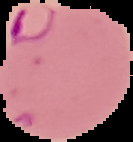
malaria status = parasitized
image type = segmented cell region with the area outside set to black
image size = 133×142 pixels
preparation = thin blood film